Assess this cell for malaria.
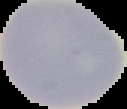
It is uninfected.

Image is 127×109 pixels. From a thin blood film. Segmented cell region on a black background.